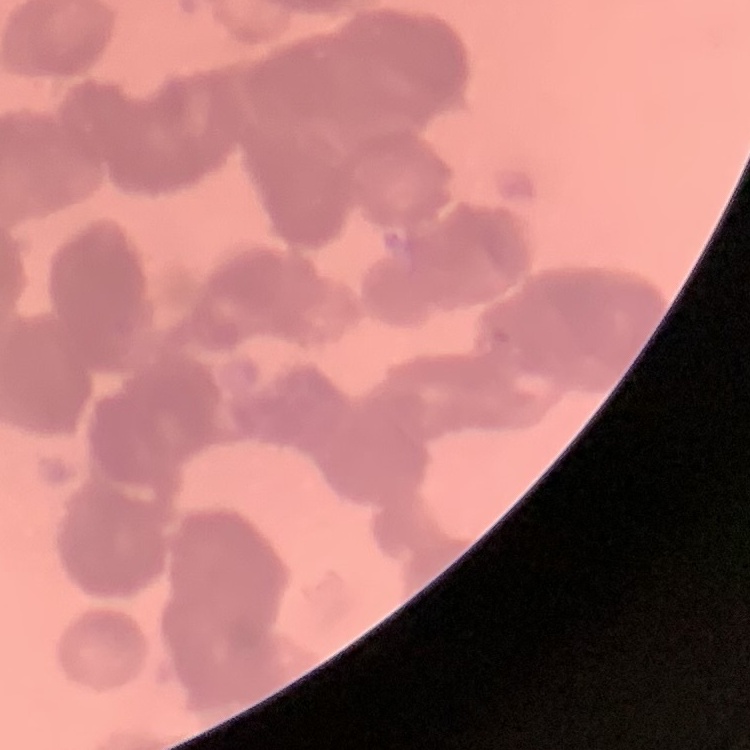

The red blood cells exhibit rouleaux formation. Thin peripheral smear. Field's or Giemsa stain. Square crop of a larger photomicrograph.